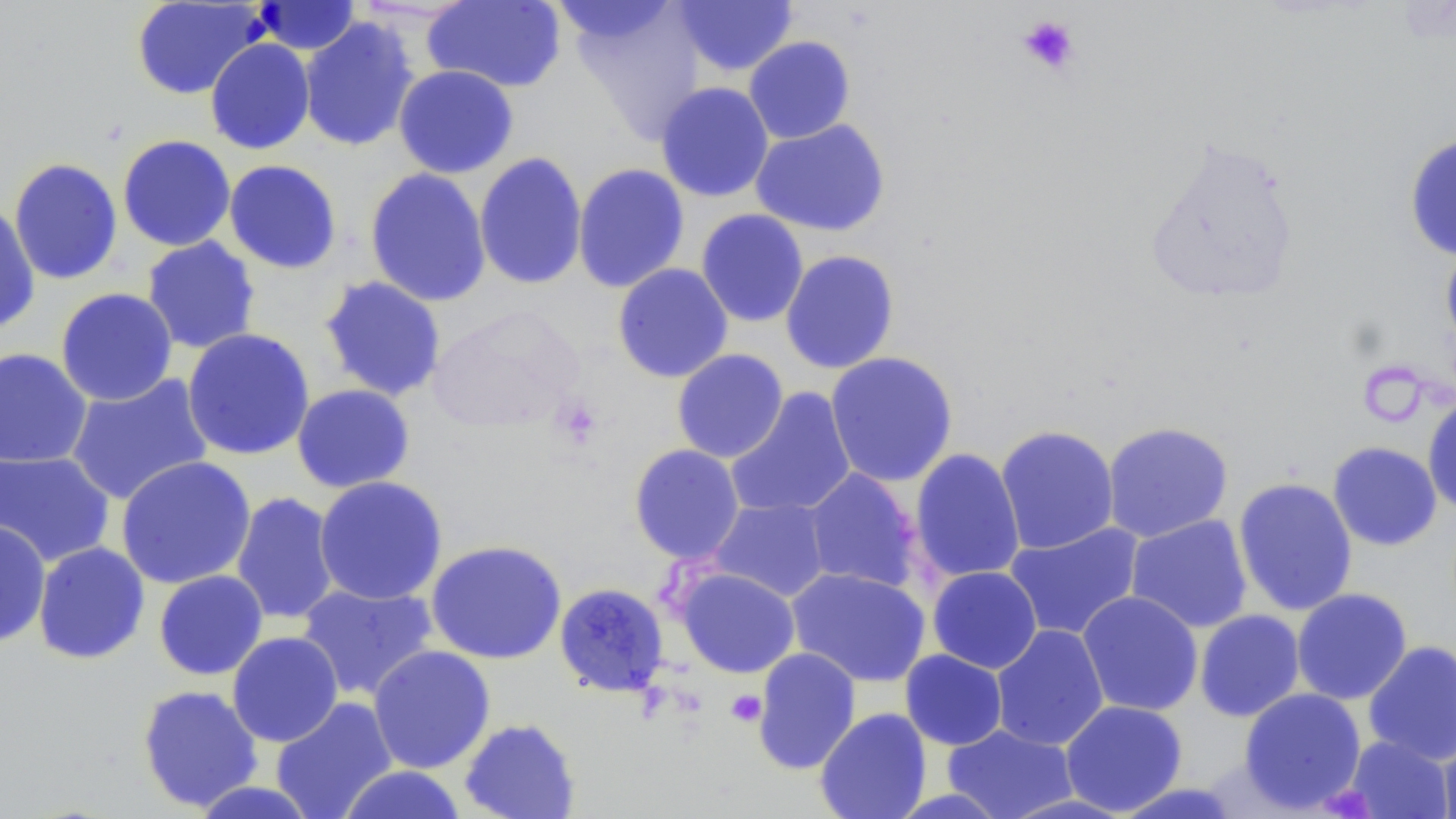

Summary:
  - Coordinate format: approximate bounding boxes as (x1,y1)-(x2,y2) corner pairs in pixels
  - Platelet locations: (1017,14)-(1080,76), (550,396)-(603,450), (726,689)-(767,727)
  - Uninfected red blood cell locations: (423,0)-(567,93), (546,0)-(683,50), (671,0)-(799,77), (131,1)-(266,100), (252,1)-(362,55), (568,3)-(707,142), (298,16)-(420,152), (743,36)-(856,144), (205,38)-(315,155), (393,65)-(519,178), (655,81)-(774,202), (750,118)-(891,237), (117,134)-(236,252), (1403,134)-(1456,262), (1143,136)-(1302,305), (9,150)-(235,269), (473,152)-(588,290), (9,158)-(123,285), (224,159)-(342,274), (572,163)-(690,293), (364,168)-(492,307), (0,202)-(41,335), (695,208)-(809,328), (141,236)-(261,354), (1440,245)-(1456,353), (779,249)-(900,374), (612,263)-(733,383), (318,275)-(448,402), (55,287)-(178,406), (426,305)-(584,433), (181,328)-(316,461), (0,347)-(92,468), (671,348)-(789,463), (824,351)-(959,488), (65,373)-(213,506), (291,383)-(415,493), (725,387)-(856,519), (1422,395)-(1456,514), (1102,421)-(1234,542), (995,425)-(1120,554), (1327,441)-(1443,551), (629,443)-(745,564), (909,448)-(1026,585), (0,449)-(116,567), (115,455)-(256,590), (802,468)-(922,594), (313,475)-(448,606), (1233,477)-(1358,616), (230,491)-(340,625), (708,497)-(831,603), (1126,514)-(1252,633), (0,520)-(51,649), (1004,522)-(1144,641), (425,539)-(567,665), (32,541)-(150,665), (927,566)-(1043,674), (675,567)-(801,678), (786,567)-(931,687), (153,569)-(269,680), (295,582)-(439,702), (554,583)-(669,698), (1291,588)-(1412,705), (1077,591)-(1204,717), (1194,609)-(1305,722), (990,624)-(1109,751), (227,631)-(344,747), (1363,640)-(1456,766), (367,645)-(496,774), (752,647)-(861,775), (900,649)-(1008,751), (137,684)-(263,813), (1239,687)-(1366,813), (271,697)-(397,819), (1060,700)-(1188,815), (814,708)-(932,819), (459,717)-(581,819), (942,724)-(1078,819), (1437,729)-(1456,819), (1345,735)-(1453,819), (338,765)-(467,819), (188,780)-(323,819)
  - Slide-level diagnosis: no evidence of blood parasites
  - Preparation: thin blood film
  - Magnification: 1000x
  - Field of view: one of a larger specimen
  - Image size: 1456×819 pixels
  - Modality: light microscopy
  - Stain: May-Grünwald-Giemsa